Identify the parasite.
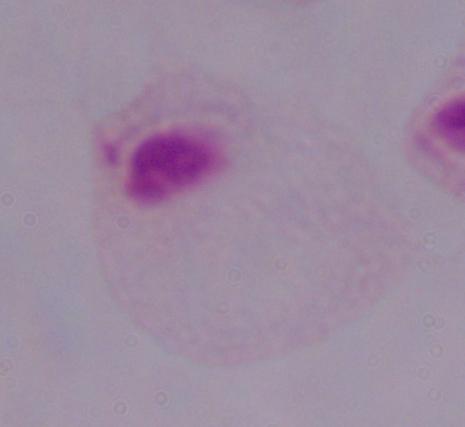

A trichomonad.

{
  "modality": "micrograph",
  "magnification": "1000x"
}